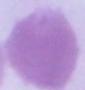

{
  "identification": "erythrocyte",
  "modality": "photomicrograph",
  "magnification": "1000x"
}